State which parasite is depicted.
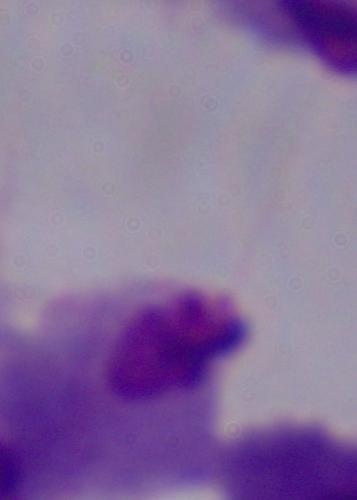

This is a trichomonad.

1000x magnification. Micrograph.